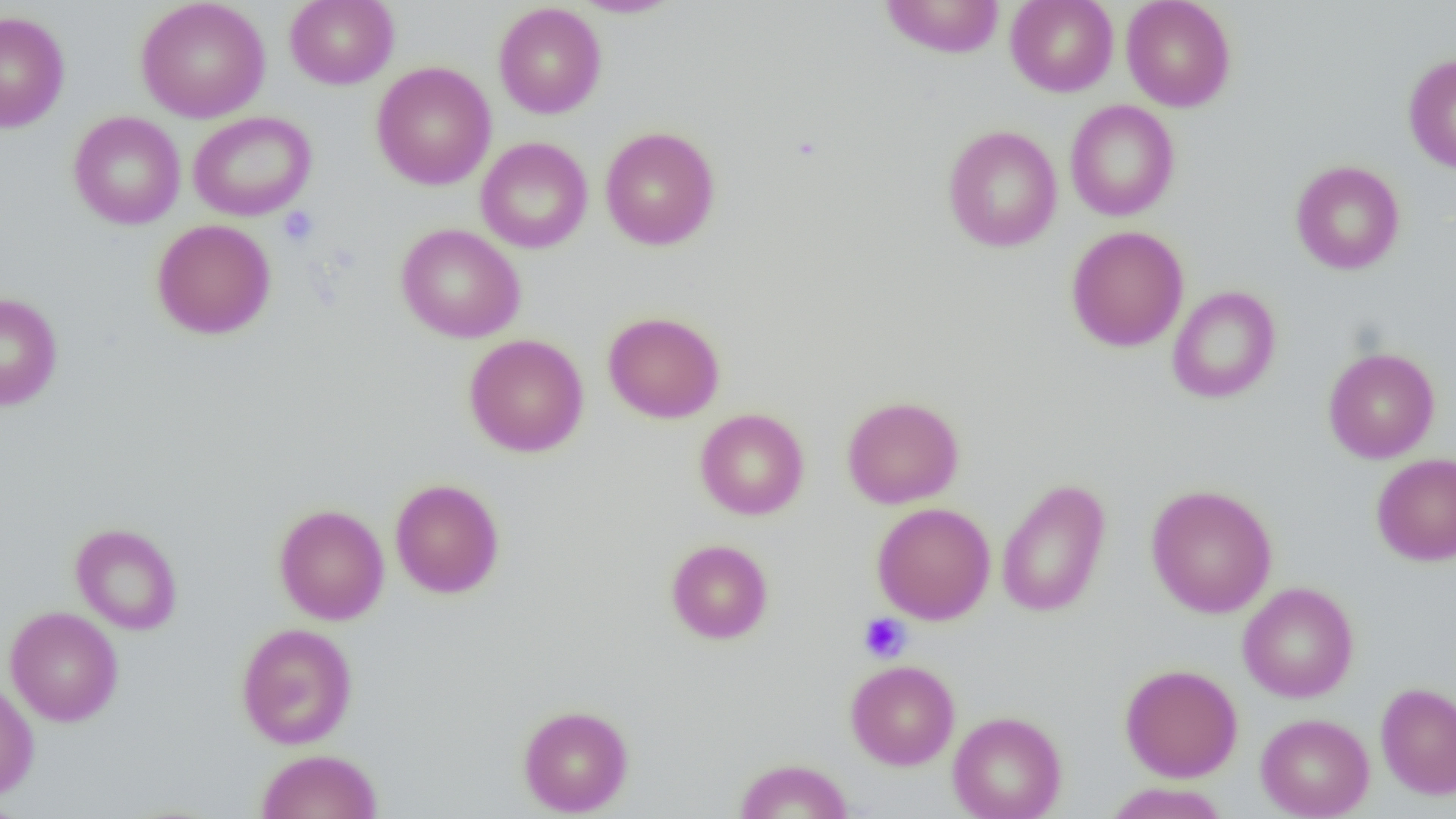
Approximate bounding boxes as [x1, y1, x2, y2] in pixels. Uninfected red blood cell locations: [135, 0, 271, 123], [284, 0, 399, 89], [571, 0, 683, 18], [880, 0, 1005, 58], [1005, 0, 1118, 97], [1121, 0, 1236, 112], [493, 2, 606, 119], [0, 11, 70, 133], [1403, 54, 1456, 172], [371, 62, 496, 190], [1065, 100, 1179, 221], [68, 111, 186, 230], [188, 111, 317, 221], [942, 125, 1063, 252], [600, 126, 720, 250], [476, 137, 593, 253], [1290, 160, 1405, 275], [151, 219, 277, 339], [395, 223, 525, 343], [1066, 226, 1189, 352], [1167, 285, 1281, 404], [0, 292, 63, 410], [603, 311, 725, 423], [464, 333, 589, 457], [1323, 346, 1440, 463], [842, 395, 964, 509], [695, 408, 809, 520], [1371, 452, 1456, 567], [389, 478, 505, 598], [996, 478, 1111, 617], [1146, 484, 1277, 618], [871, 502, 996, 624], [273, 504, 390, 625], [70, 523, 183, 635], [666, 539, 773, 644], [1238, 582, 1359, 703], [5, 606, 123, 726], [236, 622, 358, 749], [846, 659, 960, 770], [1120, 663, 1243, 782], [0, 680, 39, 800], [1376, 682, 1456, 799], [518, 704, 634, 816], [948, 711, 1067, 819], [1256, 713, 1374, 818], [255, 748, 383, 819], [733, 758, 854, 818], [1102, 782, 1230, 819], [0, 796, 26, 819]. Platelet locations: [278, 206, 319, 247], [858, 613, 912, 663]. Slide-level diagnosis: negative for blood parasites. Image is 1456×819 pixels. Thin blood film. Light microscopy. Captured at 1000x magnification. One field of a larger specimen.